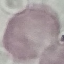

Result: no malaria parasites detected. Giemsa stain. Photographed with a smartphone camera at the microscope eyepiece. Thin blood smear. Automatically extracted cell patch, resized to 64 × 64 pixels.